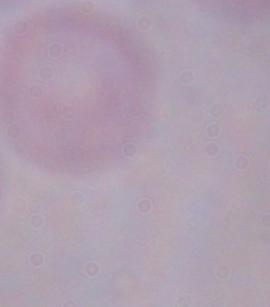

modality = micrograph
identification = trypanosome
magnification = 1000x